Comment on the morphology of the red blood cells.
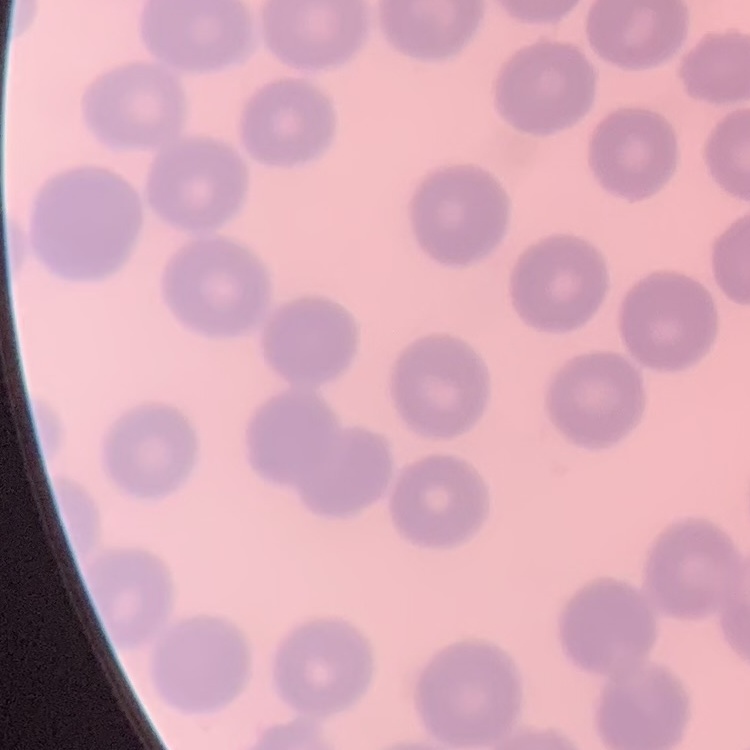
No rouleaux formation.

Field's or Giemsa stain. Square crop of a larger photomicrograph. Thin blood film.